Report the malaria status of this cell.
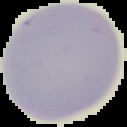

It is uninfected.

From a thin blood smear. Image is 127×127 pixels. The area outside the segmented cell region is set to black.